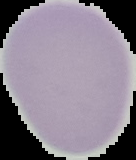
Malaria status: uninfected. From a thin blood film. Image is 136×160 pixels. Segmented cell region on a black background.